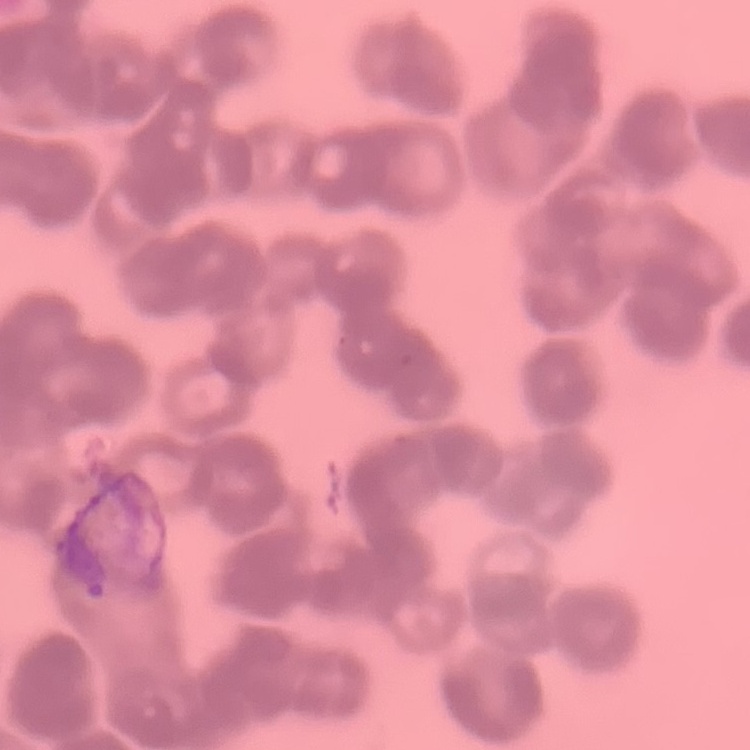

Summary:
  - Red blood cell morphology: rouleaux formation
  - Stain: Field's or Giemsa
  - Preparation: thin blood film
  - Image type: one tile cut from a larger photomicrograph